Classify this cell by malaria status.
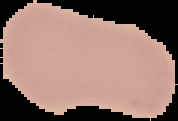

It is uninfected.

Summary:
  - Preparation: thin blood film
  - Image type: segmented cell region with the area outside set to black
  - Image size: 178×121 pixels